Point out each Plasmodium parasite and each leukocyte.
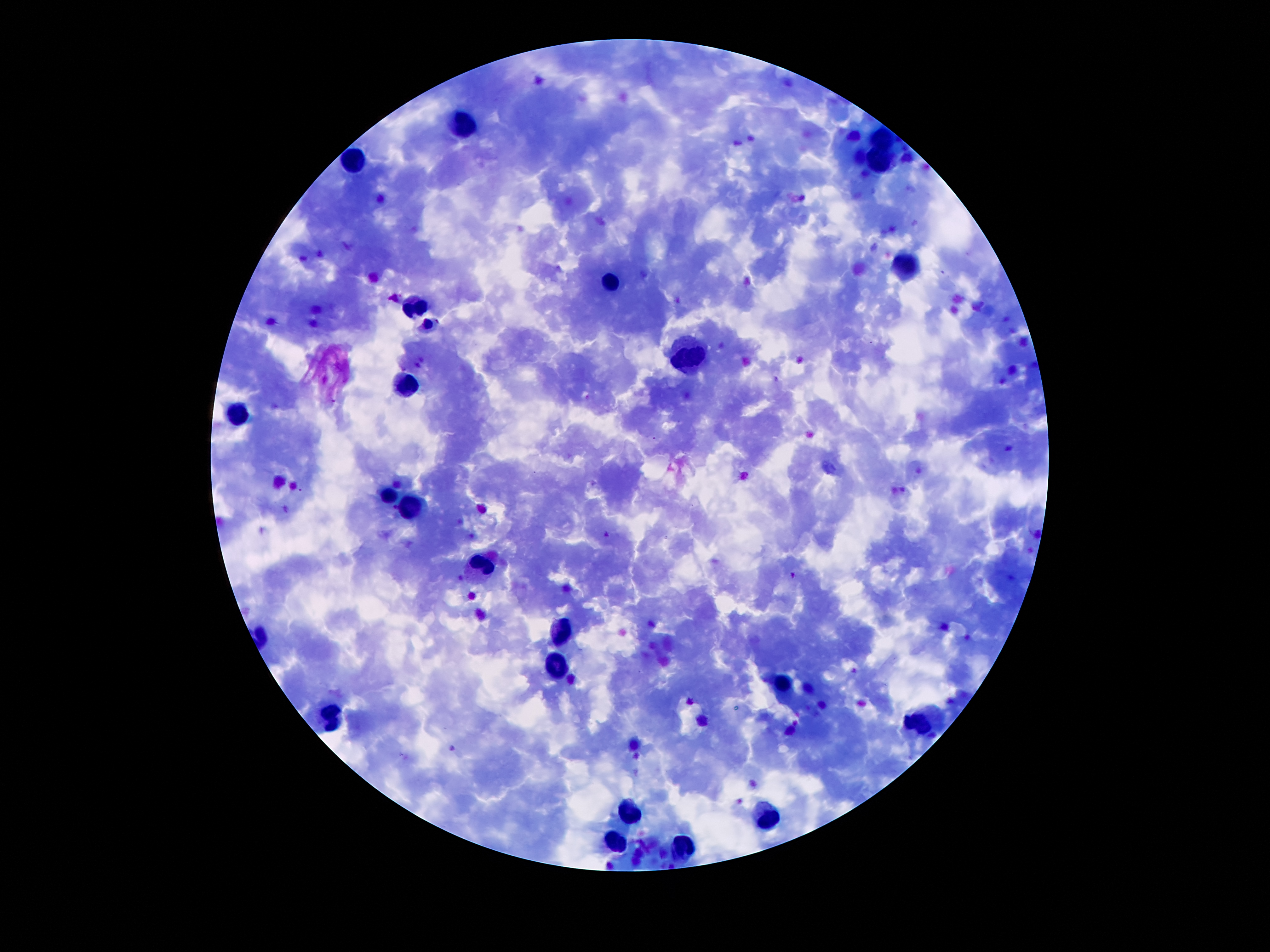

Approximate centers as (x, y) in pixels.
Plasmodium parasites: (607, 533), (793, 574).
Leukocytes: (461, 126), (883, 137), (357, 157), (881, 163), (904, 264), (609, 282), (416, 300), (688, 357), (407, 384), (238, 416), (388, 496), (413, 507), (484, 563), (563, 631), (554, 672), (784, 681), (332, 717), (922, 726), (627, 808), (770, 815), (613, 837), (684, 842).

Image is 1270×952 pixels. Single field of view. 100x magnification. Patient malaria status: infected with Plasmodium falciparum. Thick peripheral-blood smear. Photographed through the microscope eyepiece with a smartphone camera. Giemsa-stained preparation.